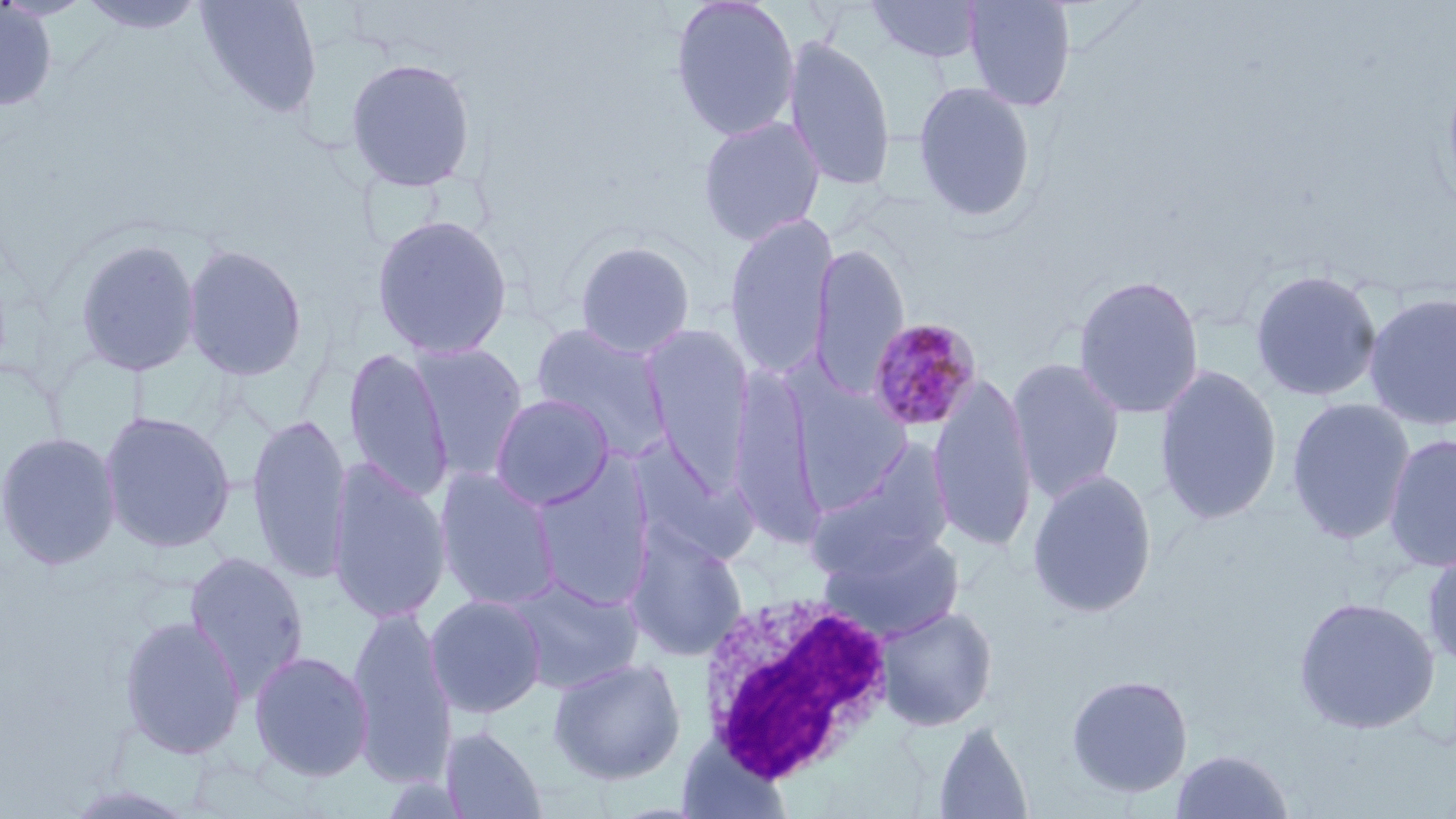 Approximate bounding boxes as named x1/y1/x2/y2 corners in pixels. White blood cell locations: (x1=696, y1=589, x2=897, y2=788). Plasmodium malariae-infected red blood cell locations: (x1=866, y1=317, x2=983, y2=434). Uninfected red blood cell locations: (x1=76, y1=0, x2=209, y2=36), (x1=194, y1=0, x2=323, y2=119), (x1=669, y1=0, x2=801, y2=142), (x1=865, y1=0, x2=986, y2=65), (x1=961, y1=0, x2=1077, y2=112), (x1=0, y1=2, x2=59, y2=113), (x1=783, y1=33, x2=896, y2=193), (x1=344, y1=56, x2=478, y2=194), (x1=913, y1=81, x2=1038, y2=222), (x1=697, y1=115, x2=826, y2=245), (x1=370, y1=212, x2=513, y2=360), (x1=723, y1=212, x2=838, y2=379), (x1=73, y1=236, x2=202, y2=378), (x1=572, y1=239, x2=696, y2=358), (x1=182, y1=242, x2=308, y2=382), (x1=809, y1=243, x2=909, y2=397), (x1=1249, y1=268, x2=1382, y2=403), (x1=1072, y1=274, x2=1205, y2=420), (x1=1363, y1=291, x2=1456, y2=431), (x1=530, y1=323, x2=671, y2=456), (x1=641, y1=325, x2=754, y2=487), (x1=409, y1=342, x2=530, y2=481), (x1=342, y1=347, x2=453, y2=502), (x1=1005, y1=357, x2=1126, y2=503), (x1=1154, y1=363, x2=1283, y2=526), (x1=728, y1=368, x2=823, y2=546), (x1=928, y1=373, x2=1038, y2=554), (x1=790, y1=379, x2=915, y2=513), (x1=490, y1=394, x2=615, y2=511), (x1=1285, y1=397, x2=1416, y2=544), (x1=98, y1=409, x2=237, y2=554), (x1=246, y1=414, x2=353, y2=586), (x1=0, y1=430, x2=121, y2=571), (x1=1383, y1=433, x2=1456, y2=573), (x1=629, y1=438, x2=757, y2=567), (x1=807, y1=444, x2=954, y2=579), (x1=326, y1=459, x2=452, y2=624), (x1=530, y1=460, x2=657, y2=610), (x1=434, y1=468, x2=561, y2=610), (x1=1026, y1=469, x2=1158, y2=619), (x1=624, y1=525, x2=749, y2=662), (x1=822, y1=530, x2=965, y2=641), (x1=1422, y1=546, x2=1456, y2=673), (x1=183, y1=551, x2=310, y2=698), (x1=506, y1=576, x2=643, y2=694), (x1=425, y1=594, x2=547, y2=718), (x1=1293, y1=596, x2=1440, y2=735), (x1=876, y1=605, x2=998, y2=731), (x1=347, y1=607, x2=455, y2=788), (x1=117, y1=614, x2=247, y2=759), (x1=248, y1=650, x2=375, y2=782), (x1=547, y1=657, x2=687, y2=785), (x1=1065, y1=674, x2=1194, y2=799), (x1=931, y1=720, x2=1034, y2=818), (x1=440, y1=724, x2=549, y2=818), (x1=1170, y1=749, x2=1295, y2=818), (x1=58, y1=784, x2=203, y2=818). Slide-level diagnosis: Plasmodium malariae. Image is 1456×819 pixels. May-Grünwald-Giemsa stain. Captured at 1000x magnification. Thin blood smear. Light microscopy. One field of a larger specimen.